Locate every blood parasite and identify its species.
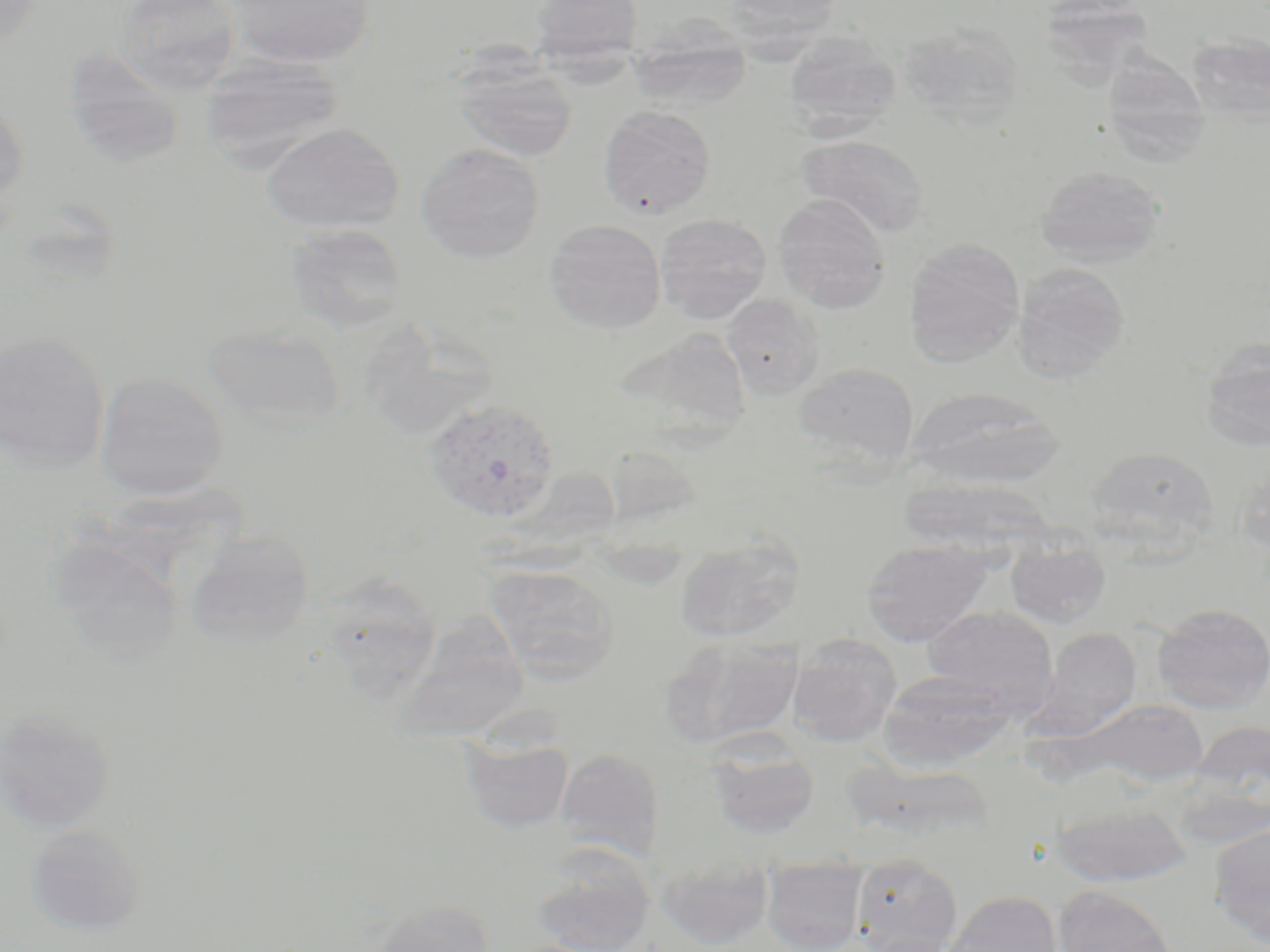

Approximate bounding boxes as named x1/y1/x2/y2 corners in pixels.
Plasmodium vivax-infected red blood cells: (x1=422, y1=397, x2=561, y2=523).
No Plasmodium falciparum, Plasmodium ovale, Plasmodium malariae, Babesia divergens, or Trypanosoma brucei observed.

Uninfected red blood cell locations: (x1=0, y1=0, x2=42, y2=53), (x1=115, y1=0, x2=244, y2=95), (x1=228, y1=0, x2=374, y2=68), (x1=529, y1=0, x2=644, y2=75), (x1=720, y1=0, x2=845, y2=38), (x1=1045, y1=0, x2=1163, y2=91), (x1=628, y1=22, x2=751, y2=113), (x1=898, y1=23, x2=1025, y2=127), (x1=1186, y1=31, x2=1270, y2=124), (x1=783, y1=32, x2=902, y2=136), (x1=60, y1=44, x2=188, y2=169), (x1=1108, y1=46, x2=1210, y2=166), (x1=198, y1=53, x2=344, y2=167), (x1=453, y1=59, x2=579, y2=163), (x1=0, y1=92, x2=29, y2=207), (x1=597, y1=105, x2=716, y2=218), (x1=259, y1=122, x2=405, y2=234), (x1=797, y1=135, x2=929, y2=237), (x1=415, y1=142, x2=546, y2=263), (x1=1036, y1=167, x2=1165, y2=266), (x1=773, y1=193, x2=892, y2=314), (x1=654, y1=214, x2=771, y2=324), (x1=543, y1=220, x2=666, y2=335), (x1=284, y1=223, x2=409, y2=333), (x1=904, y1=237, x2=1025, y2=368), (x1=1013, y1=264, x2=1129, y2=382), (x1=721, y1=295, x2=825, y2=399), (x1=371, y1=318, x2=494, y2=427), (x1=201, y1=323, x2=347, y2=434), (x1=614, y1=326, x2=753, y2=445), (x1=0, y1=330, x2=111, y2=471), (x1=1201, y1=342, x2=1270, y2=452), (x1=793, y1=362, x2=919, y2=471), (x1=95, y1=371, x2=229, y2=500), (x1=905, y1=388, x2=1065, y2=489), (x1=604, y1=444, x2=705, y2=530), (x1=1083, y1=446, x2=1219, y2=547), (x1=1234, y1=467, x2=1270, y2=559), (x1=896, y1=478, x2=1058, y2=563), (x1=184, y1=529, x2=314, y2=649), (x1=47, y1=536, x2=183, y2=665), (x1=673, y1=536, x2=804, y2=643), (x1=861, y1=538, x2=993, y2=645), (x1=1006, y1=539, x2=1111, y2=629), (x1=484, y1=564, x2=620, y2=685), (x1=316, y1=574, x2=444, y2=704), (x1=1151, y1=603, x2=1270, y2=713), (x1=922, y1=605, x2=1057, y2=712), (x1=393, y1=615, x2=530, y2=744), (x1=1032, y1=627, x2=1142, y2=738), (x1=787, y1=633, x2=902, y2=747), (x1=660, y1=635, x2=802, y2=750), (x1=878, y1=669, x2=1016, y2=769), (x1=1081, y1=699, x2=1209, y2=787), (x1=0, y1=706, x2=117, y2=834), (x1=1188, y1=719, x2=1269, y2=817), (x1=459, y1=733, x2=574, y2=834), (x1=707, y1=740, x2=820, y2=839), (x1=555, y1=748, x2=664, y2=861), (x1=843, y1=760, x2=991, y2=843), (x1=1048, y1=800, x2=1193, y2=887), (x1=1209, y1=823, x2=1270, y2=944), (x1=24, y1=824, x2=146, y2=936), (x1=527, y1=848, x2=655, y2=952), (x1=851, y1=852, x2=962, y2=952), (x1=657, y1=853, x2=773, y2=949), (x1=761, y1=857, x2=868, y2=952), (x1=1052, y1=885, x2=1178, y2=952), (x1=945, y1=890, x2=1062, y2=952), (x1=369, y1=901, x2=496, y2=952). Slide-level diagnosis: Plasmodium vivax. May-Grünwald-Giemsa stain. Thin blood smear. Captured at 1000x magnification. Single field of view. Image is 1270×952 pixels. Optical microscopy.